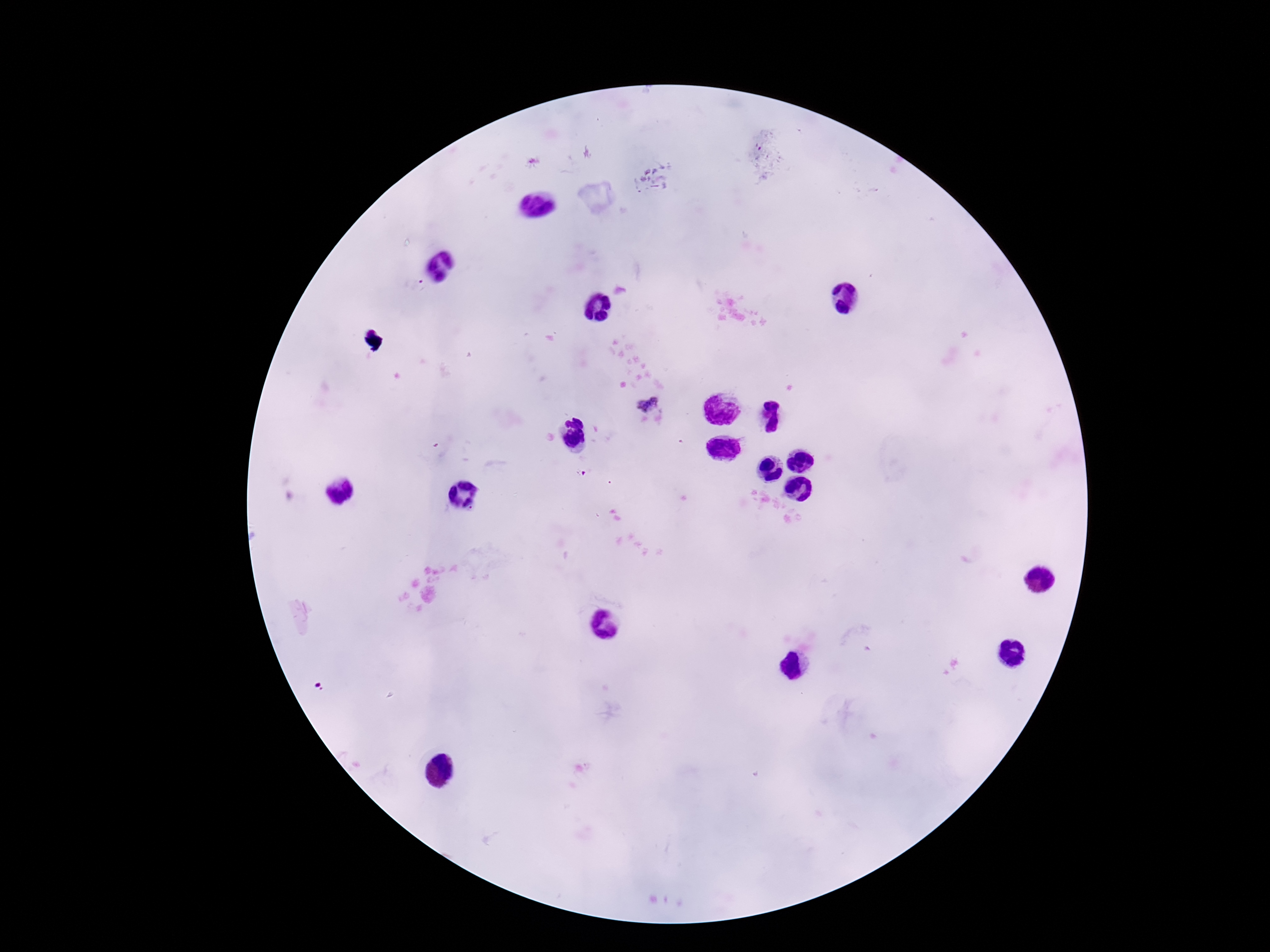
Approximate object centers, in pixels from the top-left corner.
Summary:
  - Plasmodium parasite locations: (x=648, y=400), (x=581, y=473)
  - Preparation: thick peripheral-blood smear
  - Patient malaria status: infected
  - Field of view: one from this slide
  - Image size: 1270×952 pixels
  - Stain: Giemsa
  - Capture: smartphone camera through the microscope eyepiece
  - Magnification: 100x